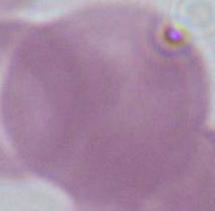

magnification: 1000x
identification: red blood cell
modality: photomicrograph